Locate every blood parasite and identify its species.
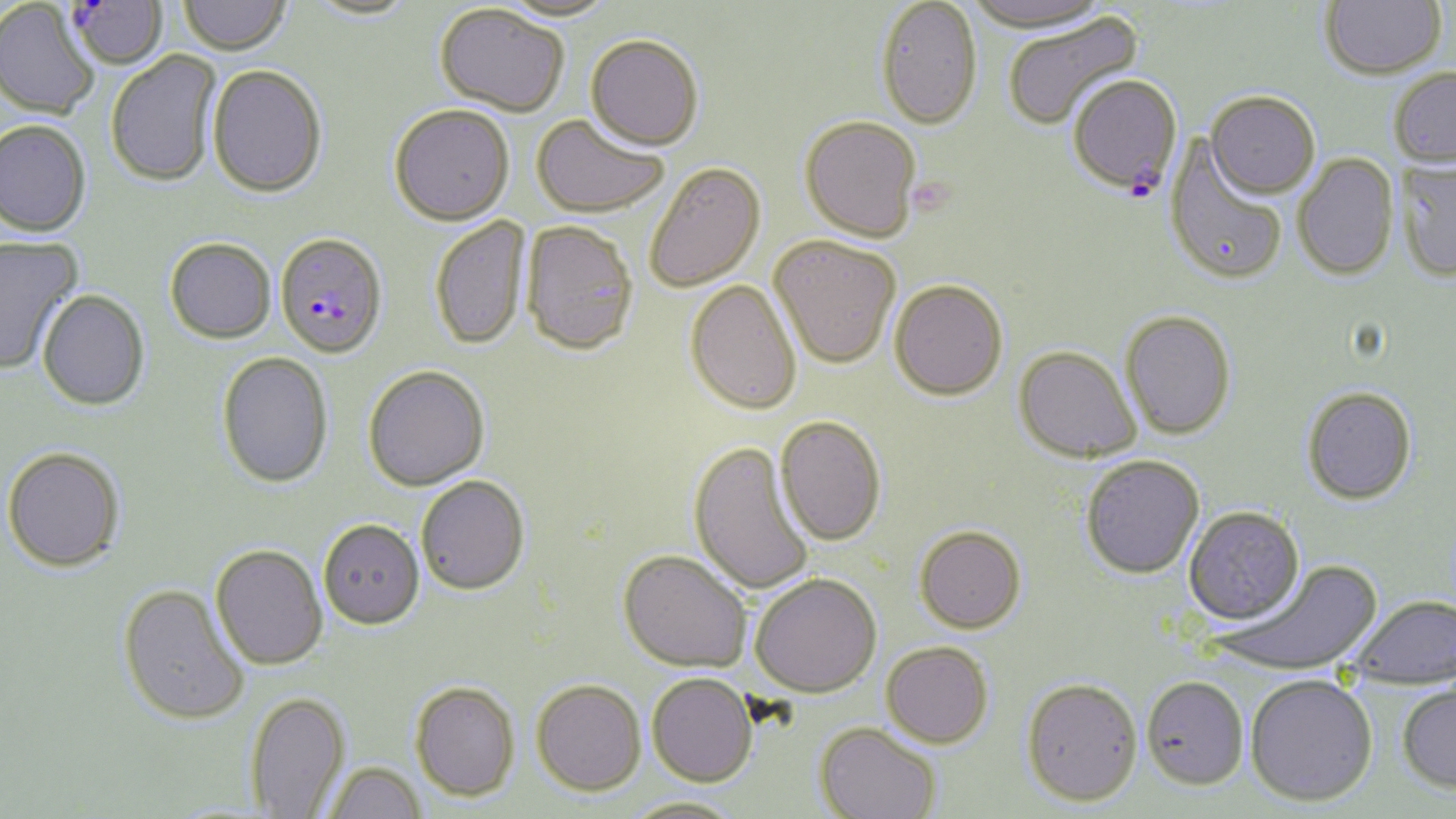
Approximate bounding boxes as named x1/y1/x2/y2 corners in pixels.
Plasmodium falciparum-infected red blood cells: (x1=65, y1=0, x2=168, y2=69), (x1=1067, y1=75, x2=1182, y2=197), (x1=275, y1=232, x2=388, y2=358).
No Plasmodium ovale, Plasmodium malariae, Plasmodium vivax, Babesia divergens, or Trypanosoma brucei observed.

Summary:
  - Uninfected red blood cell locations: (x1=178, y1=0, x2=291, y2=55), (x1=495, y1=0, x2=620, y2=22), (x1=876, y1=0, x2=983, y2=129), (x1=961, y1=0, x2=1112, y2=33), (x1=1321, y1=0, x2=1446, y2=79), (x1=304, y1=1, x2=420, y2=21), (x1=0, y1=2, x2=99, y2=120), (x1=434, y1=4, x2=570, y2=116), (x1=1001, y1=11, x2=1143, y2=132), (x1=585, y1=33, x2=704, y2=150), (x1=106, y1=50, x2=222, y2=187), (x1=207, y1=64, x2=328, y2=197), (x1=1388, y1=67, x2=1456, y2=169), (x1=1206, y1=91, x2=1321, y2=199), (x1=389, y1=103, x2=514, y2=224), (x1=531, y1=113, x2=670, y2=218), (x1=799, y1=115, x2=923, y2=242), (x1=0, y1=120, x2=91, y2=237), (x1=1164, y1=137, x2=1289, y2=287), (x1=1292, y1=153, x2=1399, y2=281), (x1=1395, y1=160, x2=1456, y2=281), (x1=643, y1=162, x2=766, y2=292), (x1=429, y1=216, x2=530, y2=350), (x1=521, y1=220, x2=640, y2=355), (x1=769, y1=235, x2=901, y2=368), (x1=0, y1=236, x2=81, y2=374), (x1=165, y1=237, x2=276, y2=343), (x1=889, y1=278, x2=1008, y2=400), (x1=685, y1=279, x2=803, y2=415), (x1=37, y1=290, x2=150, y2=411), (x1=1120, y1=310, x2=1236, y2=440), (x1=1014, y1=346, x2=1141, y2=462), (x1=217, y1=351, x2=334, y2=488), (x1=362, y1=365, x2=489, y2=491), (x1=1301, y1=386, x2=1417, y2=505), (x1=775, y1=415, x2=886, y2=545), (x1=688, y1=441, x2=815, y2=596), (x1=2, y1=446, x2=125, y2=571), (x1=1081, y1=455, x2=1204, y2=578), (x1=416, y1=475, x2=530, y2=594), (x1=1183, y1=506, x2=1304, y2=625), (x1=318, y1=518, x2=424, y2=628), (x1=914, y1=525, x2=1027, y2=633), (x1=210, y1=543, x2=328, y2=670), (x1=619, y1=549, x2=752, y2=672), (x1=1215, y1=559, x2=1382, y2=677), (x1=750, y1=572, x2=881, y2=697), (x1=118, y1=583, x2=249, y2=726), (x1=1350, y1=595, x2=1456, y2=690), (x1=881, y1=641, x2=994, y2=747), (x1=647, y1=672, x2=757, y2=786), (x1=1245, y1=673, x2=1378, y2=807), (x1=1141, y1=675, x2=1249, y2=790), (x1=1021, y1=677, x2=1142, y2=806), (x1=532, y1=678, x2=646, y2=795), (x1=409, y1=680, x2=520, y2=801), (x1=1397, y1=681, x2=1456, y2=792), (x1=245, y1=691, x2=350, y2=817), (x1=813, y1=722, x2=941, y2=818), (x1=324, y1=762, x2=427, y2=819), (x1=621, y1=797, x2=747, y2=819)
  - Slide-level diagnosis: Plasmodium falciparum
  - Field of view: single
  - Stain: May-Grünwald-Giemsa
  - Image size: 1456×819 pixels
  - Modality: light microscopy
  - Preparation: thin blood smear
  - Magnification: 1000x